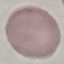
{
  "malaria_status": "uninfected",
  "stain": "Giemsa",
  "capture": "smartphone through the microscope eyepiece",
  "image_type": "cell patch, automatically extracted from a larger field of view and resized to 64 × 64 pixels",
  "preparation": "thin smear"
}